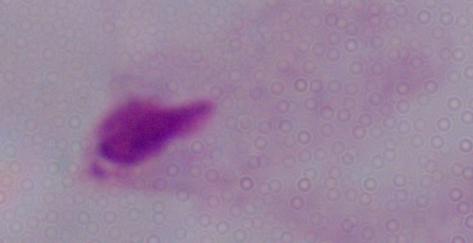
identification: trichomonad
modality: micrograph
magnification: 1000x